Outline each Plasmodium malariae-infected red blood cell.
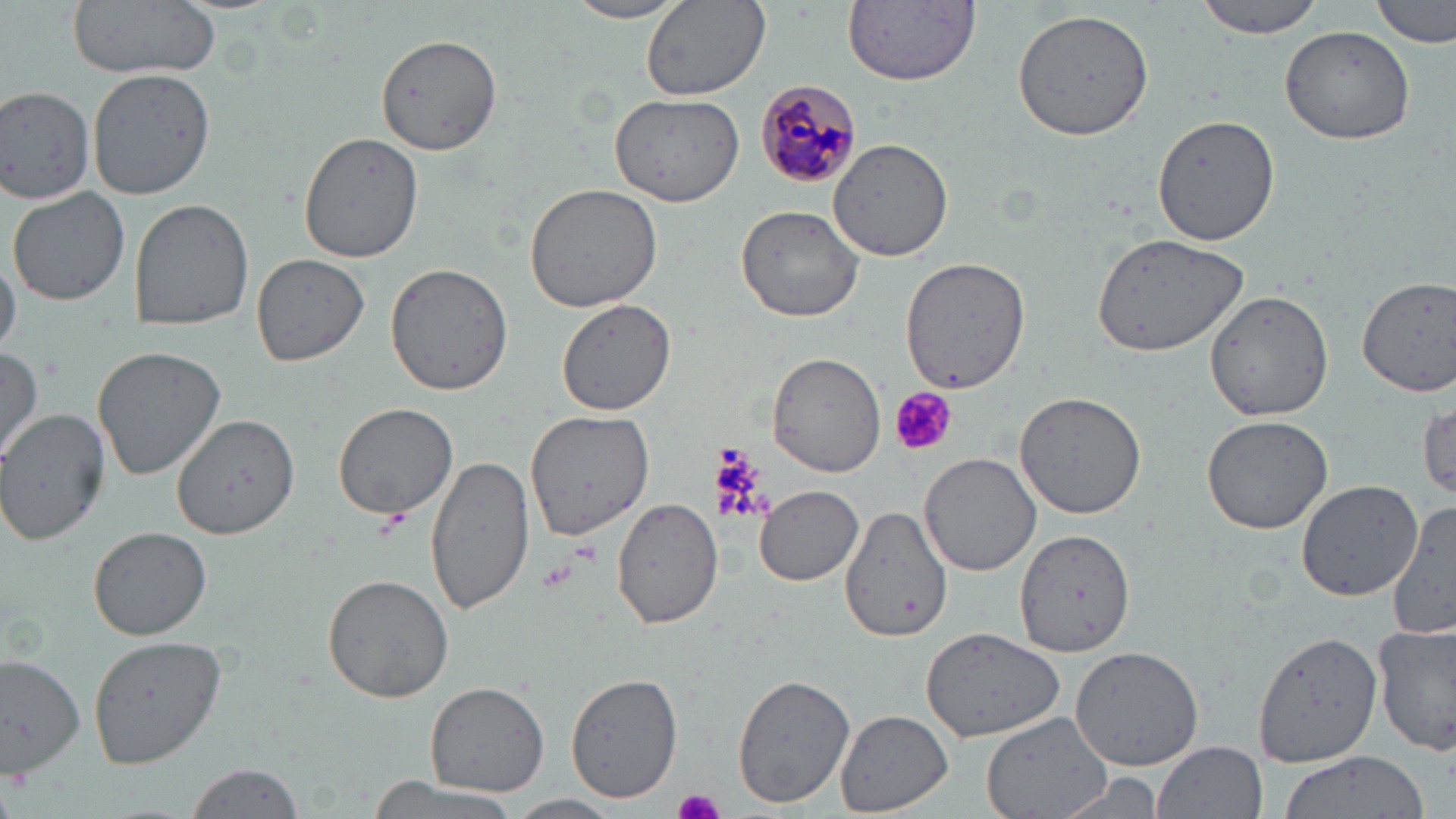

Approximate bounding boxes as named x1/y1/x2/y2 corners in pixels.
Plasmodium malariae-infected red blood cells: (x1=754, y1=76, x2=861, y2=189).

{
  "slide_level_diagnosis": "Plasmodium malariae",
  "field_of_view": "single",
  "platelet_locations": "approximate bounding boxes as named x1/y1/x2/y2 corners in pixels: (x1=891, y1=388, x2=955, y2=457), (x1=711, y1=448, x2=770, y2=526), (x1=373, y1=510, x2=410, y2=539), (x1=570, y1=541, x2=602, y2=567), (x1=675, y1=787, x2=725, y2=819)",
  "modality": "optical microscopy",
  "preparation": "thin blood smear",
  "uninfected_red_blood_cell_locations": "approximate bounding boxes as named x1/y1/x2/y2 corners in pixels: (x1=65, y1=0, x2=222, y2=79), (x1=641, y1=0, x2=771, y2=101), (x1=842, y1=0, x2=981, y2=83), (x1=1193, y1=0, x2=1326, y2=39), (x1=1372, y1=0, x2=1453, y2=47), (x1=563, y1=1, x2=691, y2=24), (x1=1013, y1=7, x2=1155, y2=141), (x1=1278, y1=26, x2=1415, y2=145), (x1=376, y1=34, x2=503, y2=155), (x1=88, y1=67, x2=217, y2=199), (x1=0, y1=85, x2=97, y2=206), (x1=609, y1=93, x2=746, y2=207), (x1=1151, y1=113, x2=1278, y2=247), (x1=297, y1=132, x2=424, y2=263), (x1=829, y1=137, x2=956, y2=261), (x1=6, y1=184, x2=131, y2=307), (x1=525, y1=184, x2=663, y2=314), (x1=128, y1=199, x2=254, y2=332), (x1=733, y1=203, x2=865, y2=323), (x1=1089, y1=231, x2=1254, y2=357), (x1=0, y1=252, x2=22, y2=357), (x1=250, y1=252, x2=370, y2=367), (x1=900, y1=256, x2=1032, y2=396), (x1=384, y1=262, x2=515, y2=395), (x1=1356, y1=276, x2=1456, y2=397), (x1=1205, y1=289, x2=1334, y2=421), (x1=557, y1=300, x2=676, y2=415), (x1=0, y1=345, x2=45, y2=465), (x1=92, y1=346, x2=226, y2=481), (x1=768, y1=353, x2=887, y2=477), (x1=1016, y1=391, x2=1145, y2=518), (x1=167, y1=397, x2=299, y2=534), (x1=1416, y1=397, x2=1455, y2=506), (x1=331, y1=400, x2=458, y2=519), (x1=1, y1=408, x2=111, y2=546), (x1=524, y1=408, x2=654, y2=540), (x1=1201, y1=415, x2=1333, y2=533), (x1=918, y1=452, x2=1040, y2=576), (x1=425, y1=454, x2=535, y2=614), (x1=1294, y1=477, x2=1426, y2=601), (x1=754, y1=483, x2=864, y2=586), (x1=610, y1=496, x2=725, y2=630), (x1=1388, y1=503, x2=1455, y2=645), (x1=837, y1=506, x2=957, y2=647), (x1=89, y1=526, x2=212, y2=640), (x1=1017, y1=529, x2=1135, y2=657), (x1=323, y1=574, x2=454, y2=702), (x1=920, y1=626, x2=1066, y2=746), (x1=1372, y1=626, x2=1456, y2=758), (x1=1252, y1=631, x2=1383, y2=768), (x1=86, y1=634, x2=227, y2=767), (x1=1069, y1=644, x2=1207, y2=772), (x1=0, y1=655, x2=86, y2=775), (x1=731, y1=673, x2=856, y2=809), (x1=566, y1=674, x2=683, y2=805), (x1=426, y1=681, x2=549, y2=797), (x1=836, y1=709, x2=954, y2=817), (x1=980, y1=709, x2=1117, y2=819), (x1=1153, y1=741, x2=1267, y2=819), (x1=1275, y1=751, x2=1429, y2=818), (x1=186, y1=762, x2=307, y2=818), (x1=1049, y1=773, x2=1171, y2=819), (x1=360, y1=775, x2=530, y2=819), (x1=505, y1=793, x2=625, y2=819)",
  "magnification": "1000x",
  "stain": "May-Grünwald-Giemsa",
  "image_size": "1456×819 pixels"
}